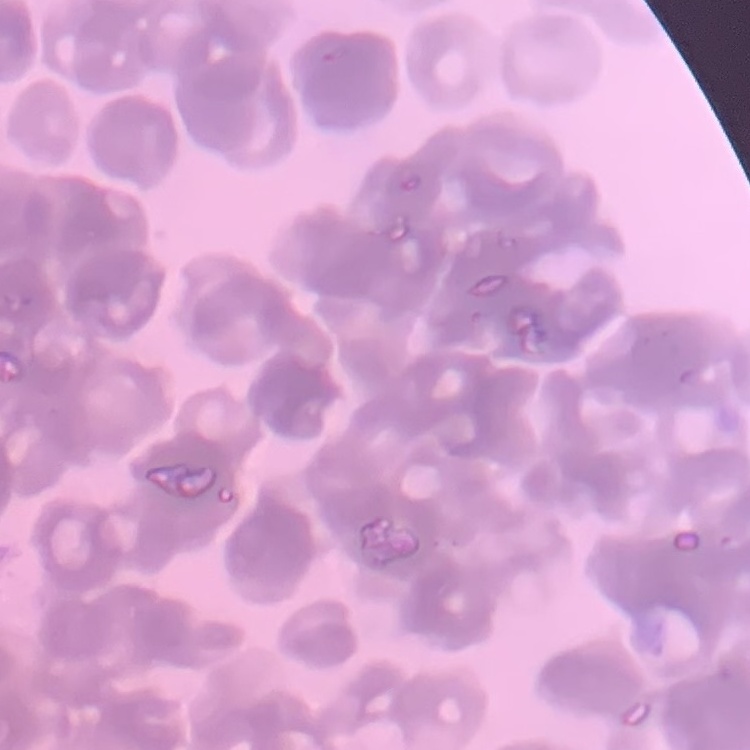 The red blood cells exhibit rouleaux formation. Stained with either Field's or Giemsa. Thin peripheral smear. Square crop of a larger photomicrograph.